Locate every Plasmodium parasite.
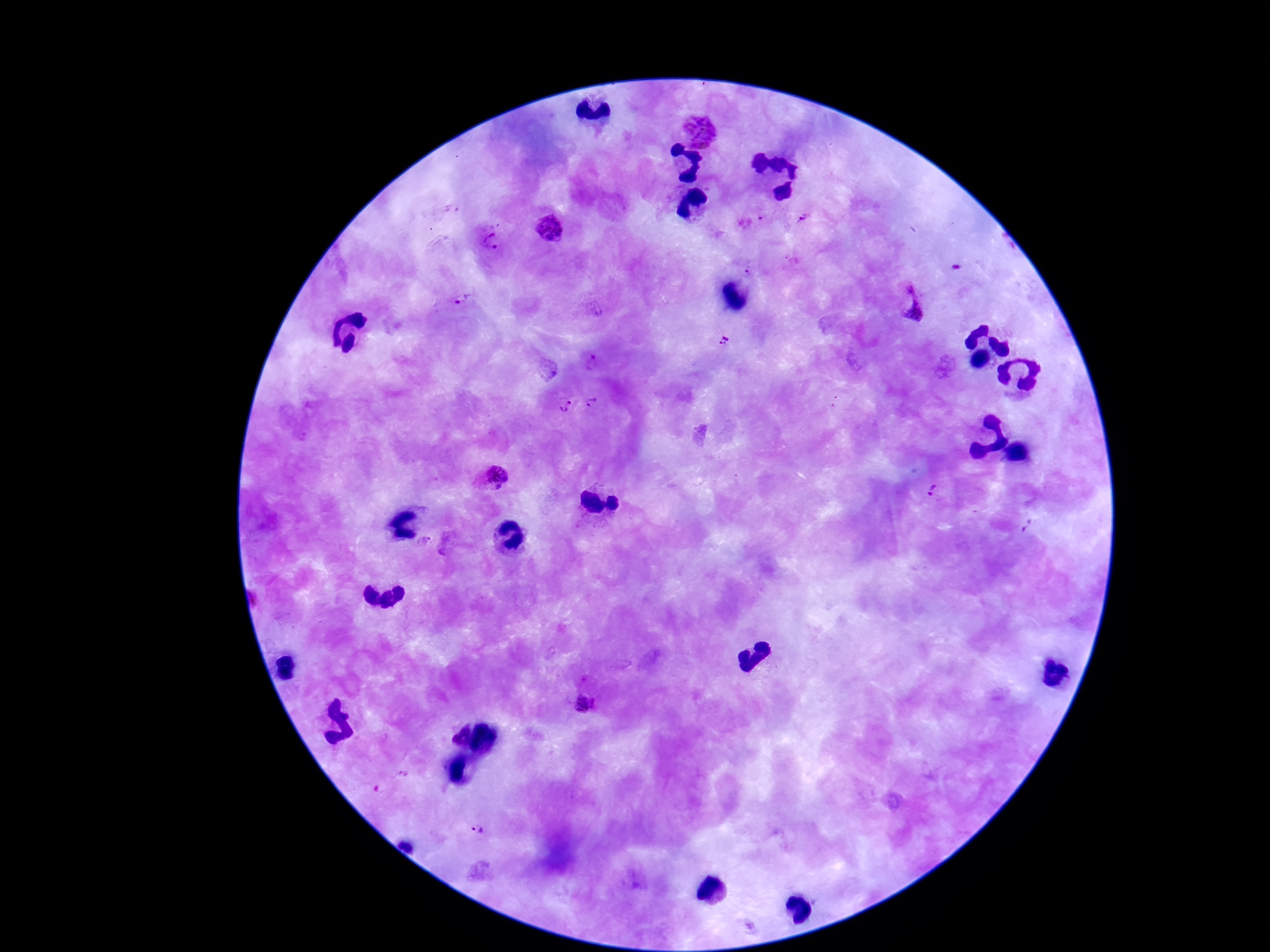

Approximate centers as [x, y] in pixels.
Plasmodium parasites: [697, 131], [804, 218], [751, 223], [552, 227], [492, 241], [749, 273], [915, 299], [464, 302], [724, 340], [592, 364], [564, 403], [592, 404], [492, 479], [931, 491], [586, 706], [478, 829].

magnification = 100x
image size = 1270×952 pixels
patient malaria status = infected
field of view = one from this slide
stain = Giemsa
preparation = thick blood smear
capture = smartphone camera through the microscope eyepiece